Assess the morphology of the red blood cells.
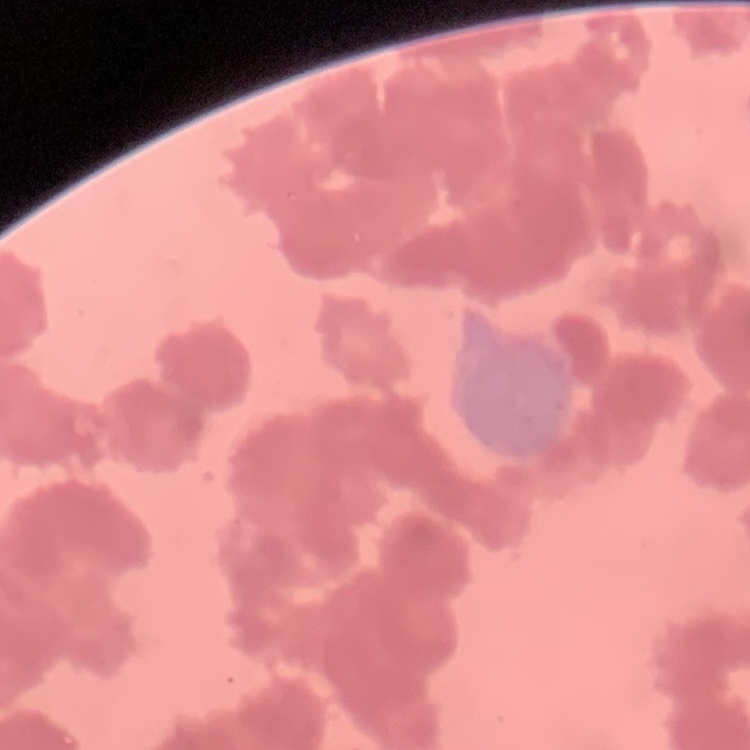
Rouleaux formation.

image_type: one tile cut from a larger photomicrograph
preparation: thin blood film
stain: Field's or Giemsa